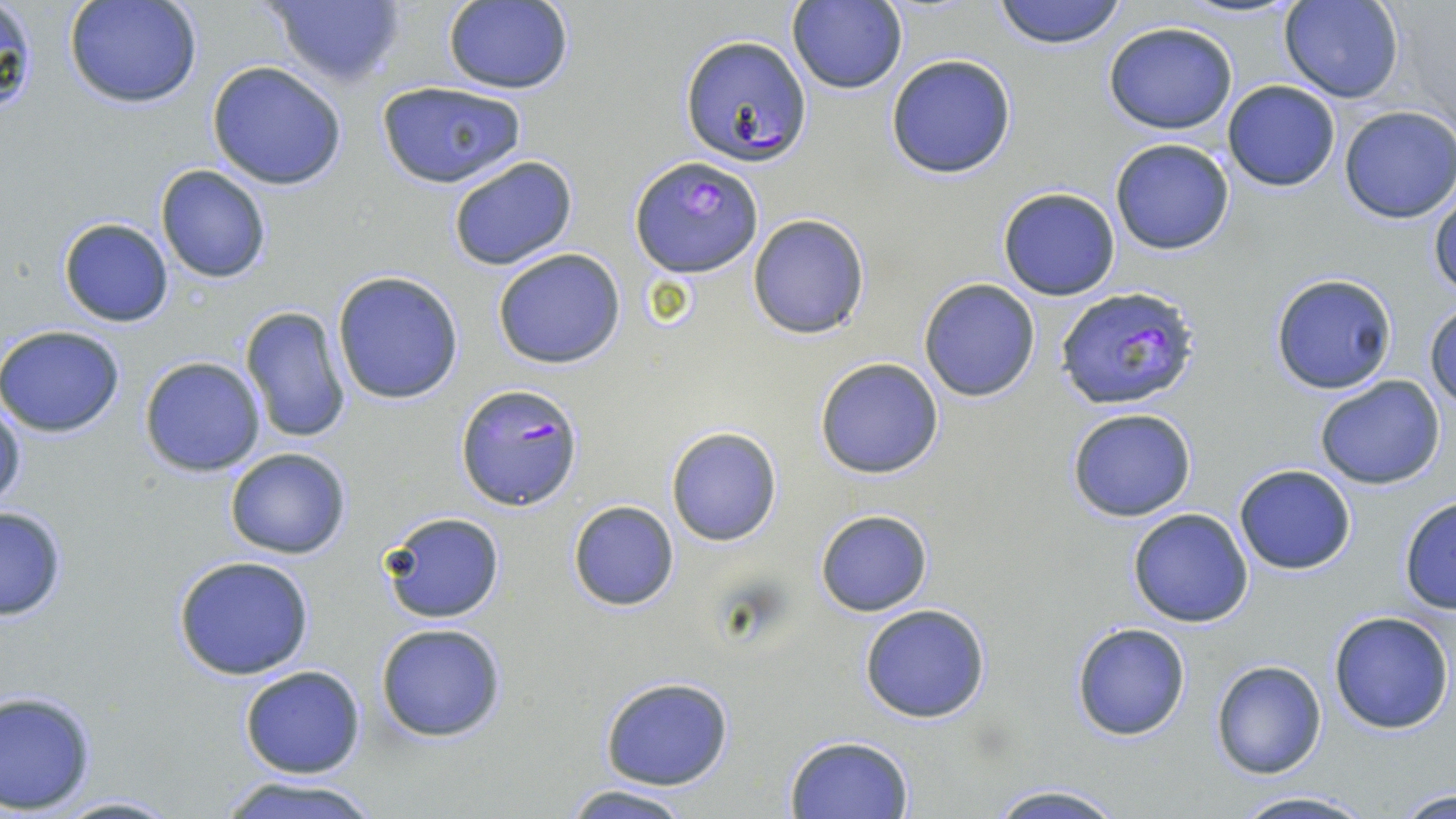 Approximate bounding boxes as (x1,y1)-(x2,y2) corner pairs in pixels. Uninfected red blood cell locations: (64,0)-(204,109), (264,0)-(405,90), (993,0)-(1128,50), (1279,0)-(1402,103), (2,1)-(37,116), (787,1)-(908,95), (440,2)-(575,93), (1103,20)-(1239,134), (884,53)-(1017,180), (205,61)-(349,190), (375,79)-(530,190), (1222,80)-(1341,191), (1337,106)-(1455,224), (1109,137)-(1237,256), (447,154)-(577,271), (155,163)-(272,284), (1429,184)-(1456,299), (996,186)-(1121,301), (747,212)-(871,340), (56,216)-(176,328), (493,248)-(626,369), (332,271)-(464,405), (1269,272)-(1398,395), (918,277)-(1042,402), (1425,302)-(1456,411), (240,305)-(354,444), (0,324)-(126,438), (138,355)-(267,477), (814,356)-(946,479), (1314,376)-(1446,490), (1,396)-(25,511), (1066,407)-(1197,522), (665,424)-(783,546), (224,447)-(351,559), (1233,463)-(1357,574), (1397,495)-(1456,613), (566,499)-(680,611), (0,505)-(69,621), (815,508)-(934,617), (1128,508)-(1255,628), (378,510)-(506,624), (171,556)-(317,680), (858,603)-(992,724), (1328,609)-(1456,734), (1070,621)-(1191,742), (374,622)-(507,743), (1210,659)-(1326,780), (239,665)-(365,778), (599,677)-(735,789), (0,689)-(99,813), (784,735)-(915,817), (213,773)-(383,819), (984,783)-(1130,819), (560,785)-(697,819), (1386,785)-(1456,818), (1224,792)-(1378,819), (44,793)-(187,818). Plasmodium falciparum-infected red blood cell locations: (679,34)-(812,167), (631,155)-(764,279), (1055,284)-(1201,413), (456,383)-(584,510). Slide-level diagnosis: Plasmodium falciparum. Captured at 1000x magnification. Optical microscopy. Image is 1456×819 pixels. One field of a larger specimen. May-Grünwald-Giemsa-stained preparation. Thin blood film.